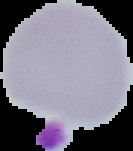 Cell region segmented out of the field of view; the surrounding area is masked to black. Image is 133×151 pixels. From a thin blood smear. Malaria status: uninfected.